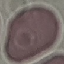

Malaria status: uninfected. Acquired by smartphone through the microscope eyepiece. Giemsa-stained preparation. Thin blood film. Automatically extracted cell patch, resized to 64 × 64 pixels.